Identify the parasite.
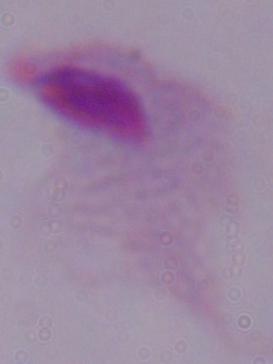

A trichomonad.

Summary:
  - Modality: micrograph
  - Magnification: 1000x